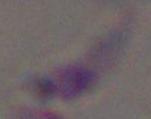
Photomicrograph. Toxoplasma gondii is seen. 1000x magnification.